State which parasite is depicted.
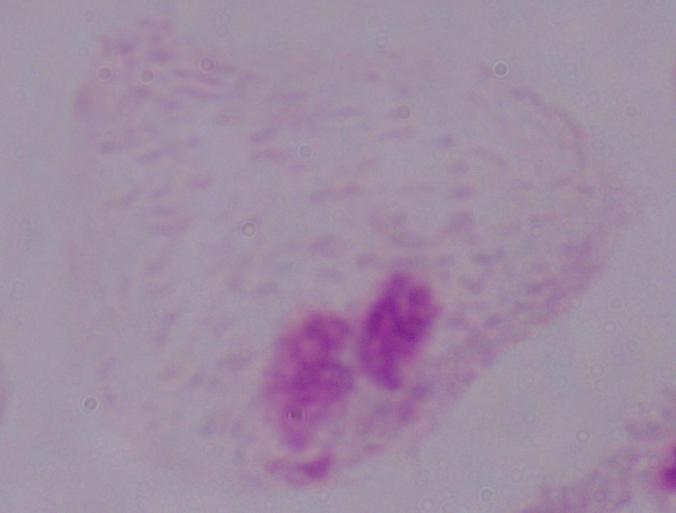
This is a trichomonad.

modality = micrograph
magnification = 1000x